Assess this cell for malaria.
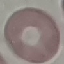

Uninfected.

stain = Giemsa
preparation = thin smear
image type = automatically extracted cell patch, resized to 64 × 64 pixels
capture = smartphone through the microscope eyepiece